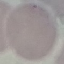
Summary:
  - Malaria status: uninfected
  - Image type: cell patch, automatically extracted from a larger field of view and resized to 64 × 64 pixels
  - Preparation: thin blood smear
  - Capture: smartphone camera at the microscope eyepiece
  - Stain: Giemsa